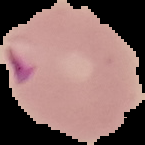

Summary:
  - Result: Plasmodium parasites identified
  - Preparation: thin blood film
  - Image size: 145×145 pixels
  - Image type: segmented cell region on a black background